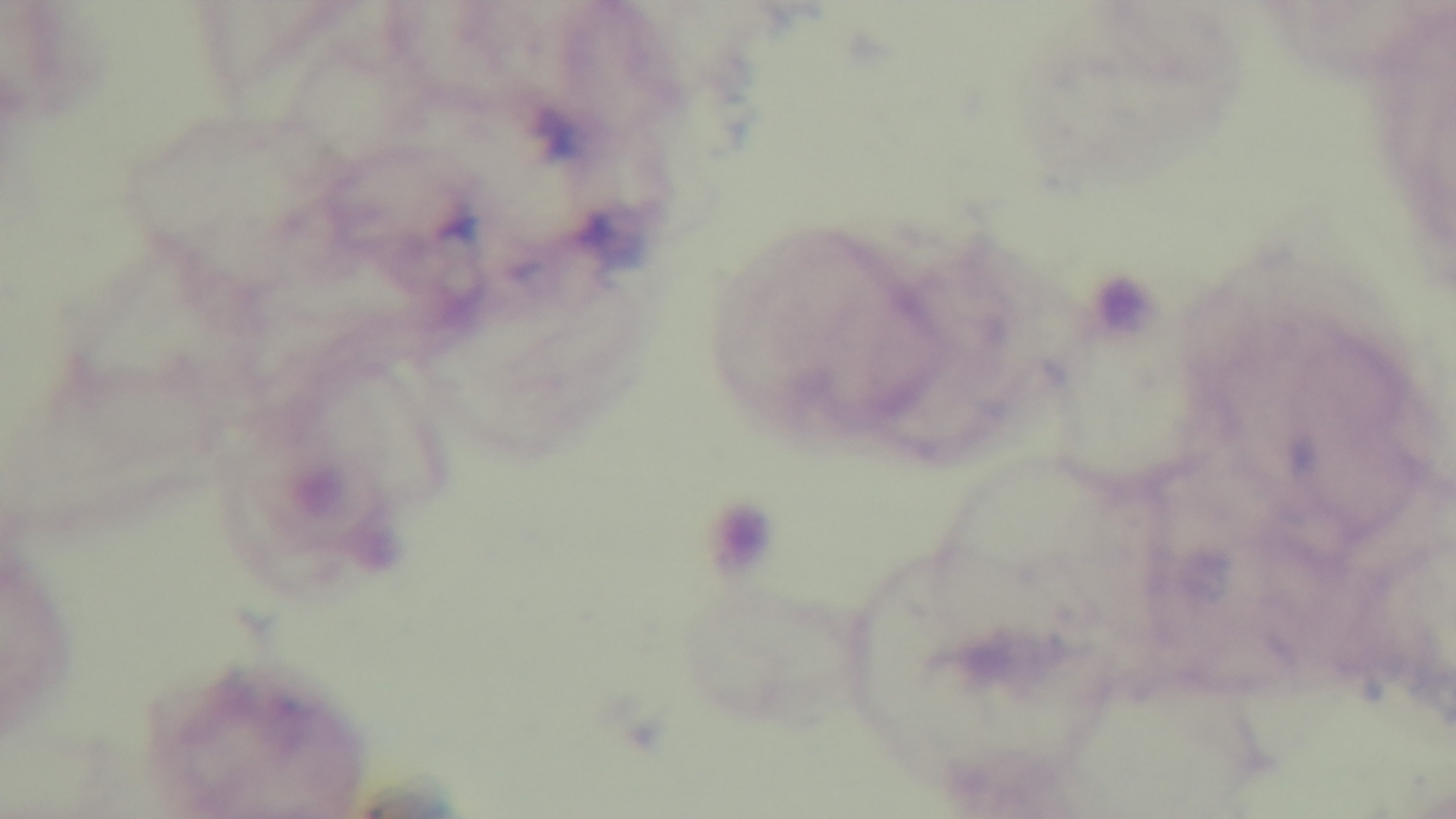

Giemsa-stained. 100x oil-immersion objective. Single field of view. Preparation: thick blood film. Photomicrograph. Malaria status: uninfected. Mounted 4K digital camera.